Describe the morphology of the erythrocytes.
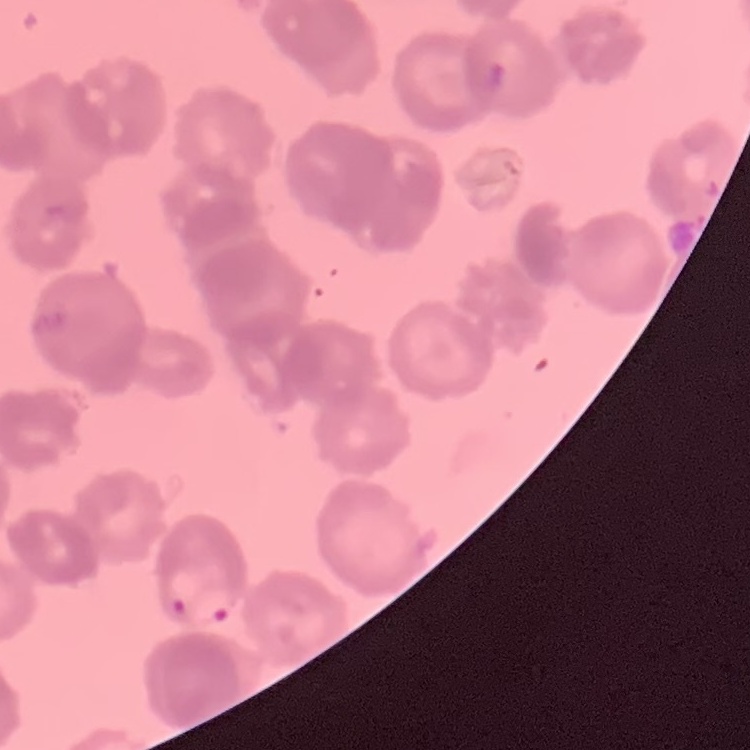
Rouleaux formation.

Summary:
  - Image type: square crop of a larger photomicrograph
  - Preparation: thin blood film
  - Stain: Field's or Giemsa